Describe the morphology of the erythrocytes.
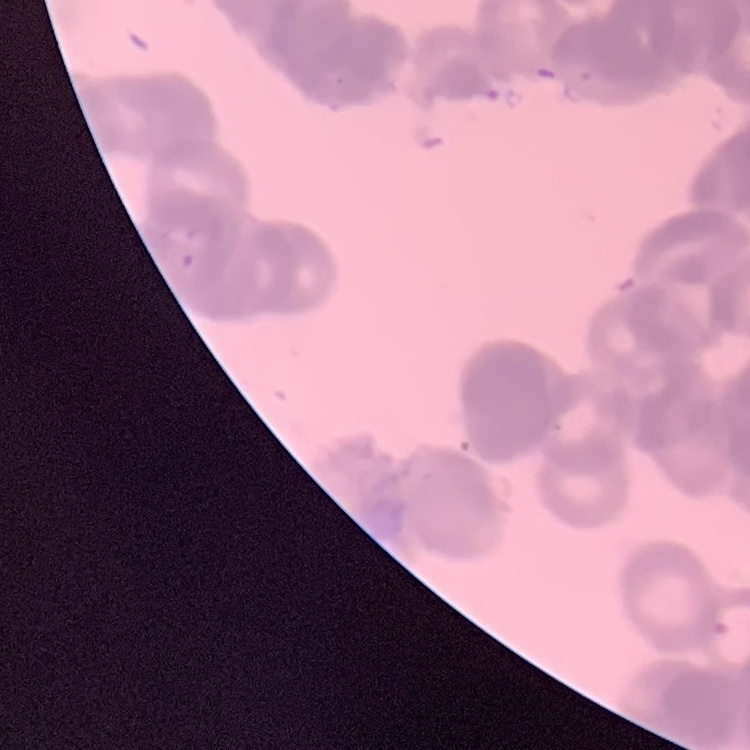

Rouleaux formation.

Field's or Giemsa stain. One tile cut from a larger photomicrograph. Thin blood smear.